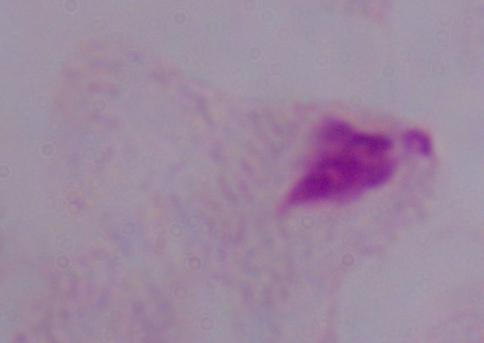 Photomicrograph. A trichomonad is seen. 1000x magnification.